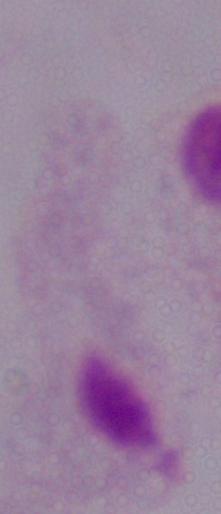
Photomicrograph. 1000x magnification. A trichomonad is shown.